Identify the preparation type.
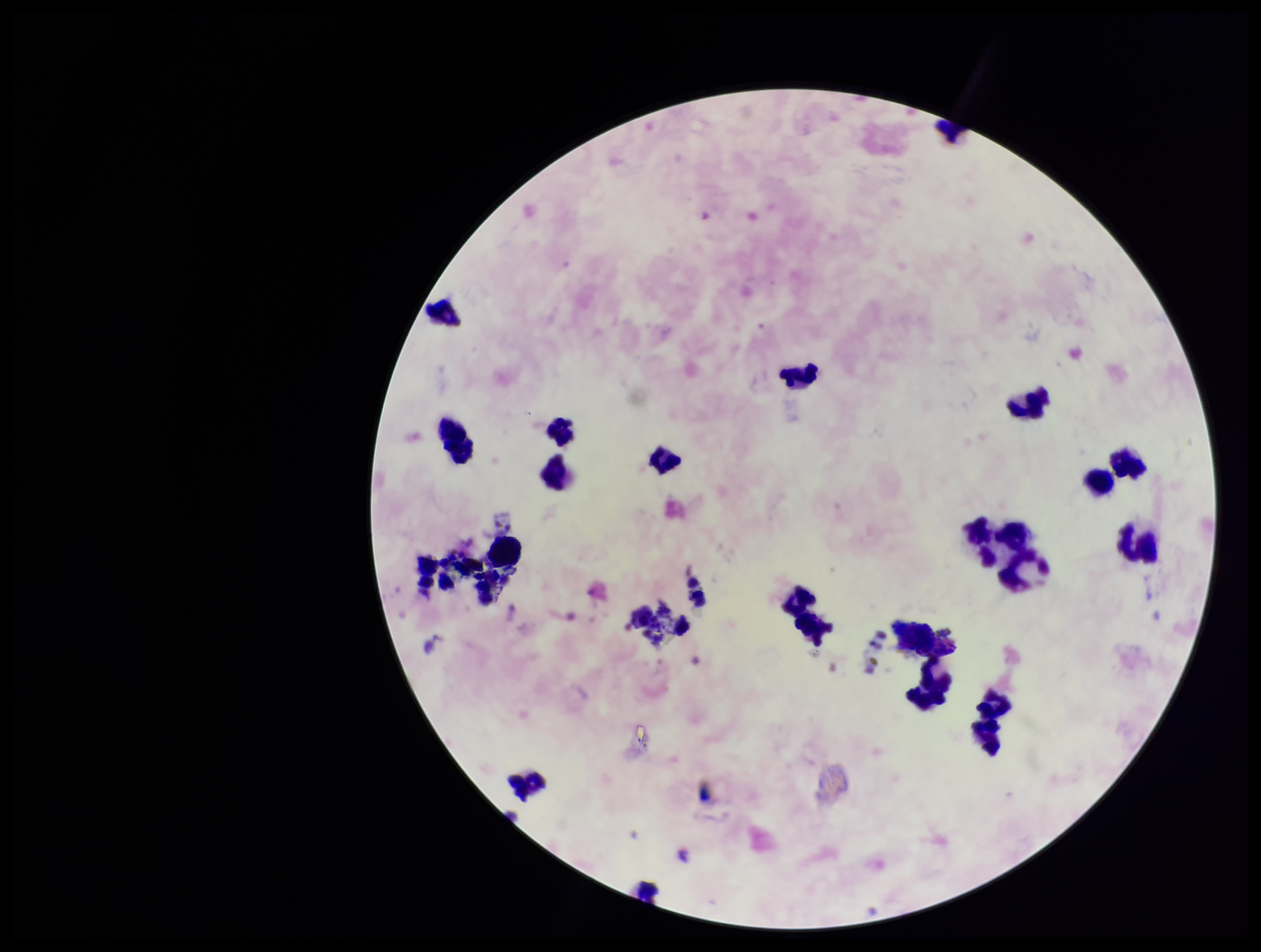

Thick.

Photographed through the microscope eyepiece with a smartphone camera. Single field of view. Patient malaria status: negative. Image is 1261×952 pixels. Parasite count: 0. Leukocyte count: 23. Plasmodium parasites: none detected. Giemsa stain.